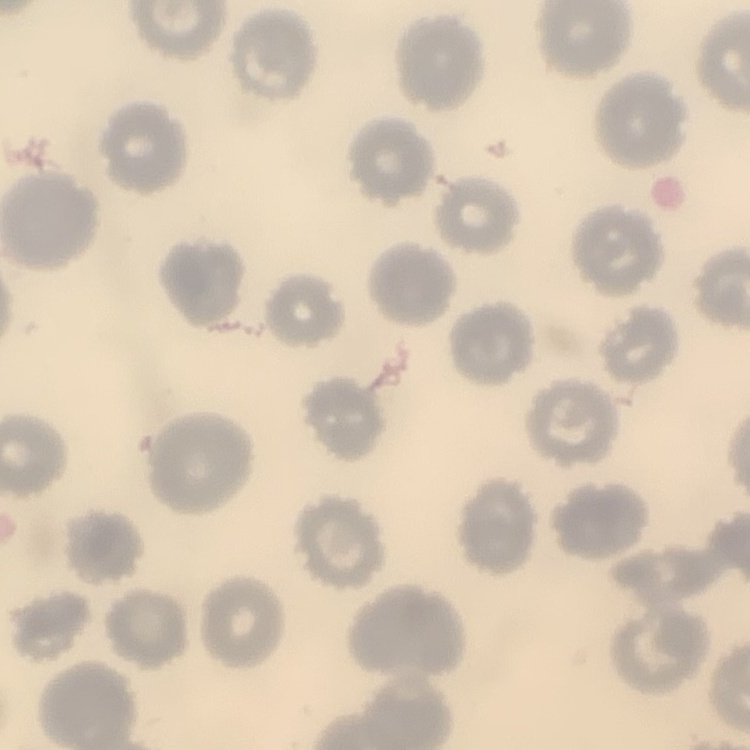 The red blood cells show no rouleaux formation. Stained with either Field's or Giemsa. One tile cut from a larger photomicrograph. Thin peripheral smear.